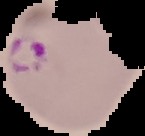
The area outside the segmented cell region is set to black. Image is 145×136 pixels. Result: malaria parasites detected. From a thin blood smear.